Name the blood parasite species.
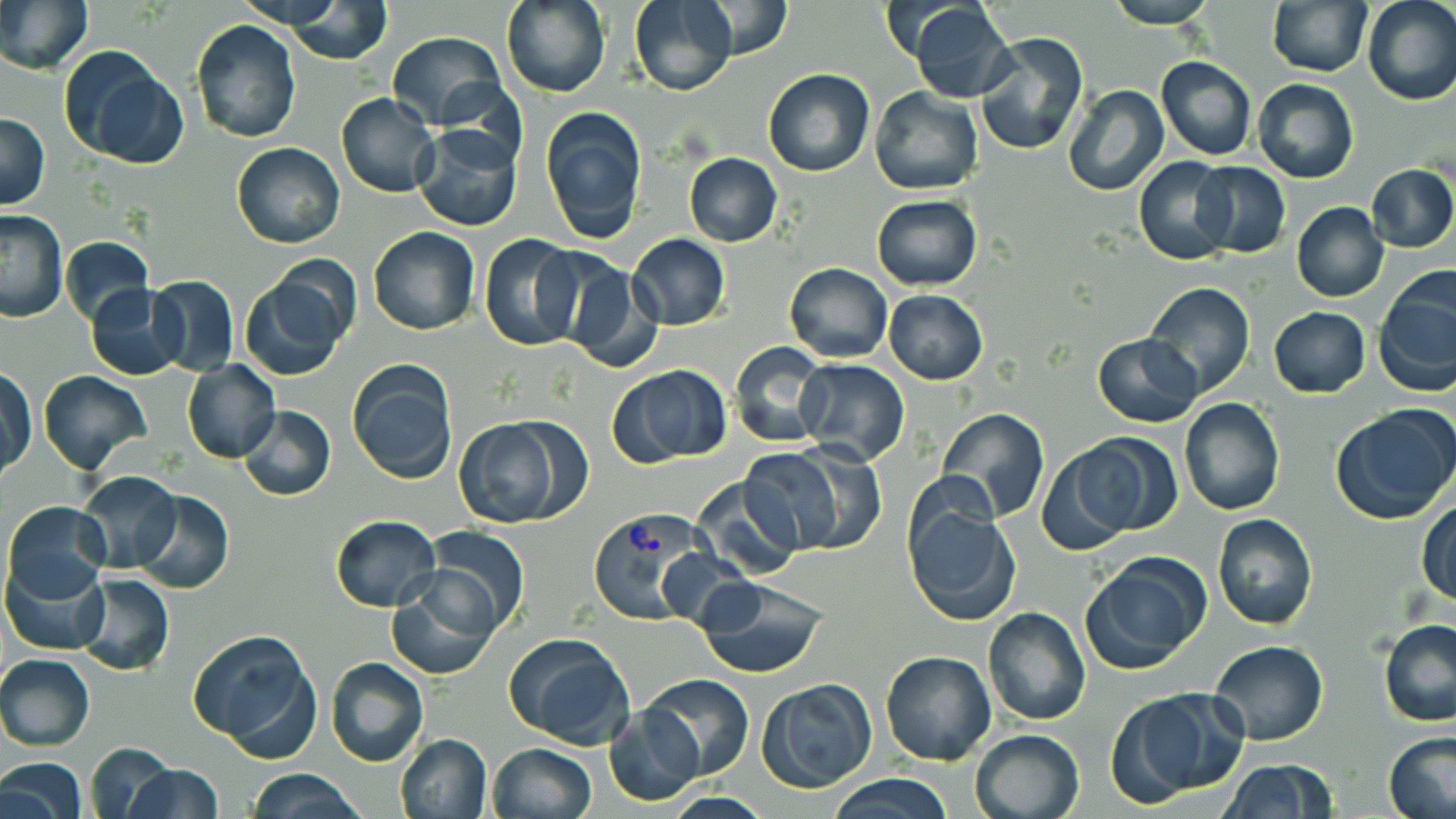
Plasmodium vivax.

Approximate bounding boxes as [x1, y1, x2, y2] in pixels. Uninfected red blood cell locations: [0, 0, 91, 75], [231, 0, 355, 32], [500, 0, 611, 98], [629, 0, 738, 95], [1103, 0, 1218, 27], [1361, 0, 1455, 107], [692, 1, 792, 62], [907, 1, 1019, 103], [1267, 1, 1372, 76], [285, 2, 390, 65], [191, 19, 301, 143], [386, 31, 507, 129], [975, 31, 1088, 156], [59, 47, 188, 169], [1155, 56, 1257, 160], [763, 67, 875, 177], [1252, 79, 1359, 185], [1064, 85, 1169, 198], [869, 86, 983, 195], [335, 92, 439, 198], [540, 106, 648, 243], [0, 112, 49, 209], [411, 124, 523, 232], [231, 141, 345, 249], [683, 152, 782, 247], [1133, 156, 1236, 266], [1192, 161, 1291, 258], [1367, 163, 1456, 253], [870, 195, 982, 289], [1291, 203, 1389, 302], [0, 211, 68, 323], [368, 226, 479, 335], [479, 232, 586, 351], [627, 233, 730, 331], [61, 237, 151, 326], [557, 260, 664, 373], [784, 263, 892, 362], [240, 273, 351, 380], [1375, 274, 1456, 399], [145, 275, 239, 374], [1143, 282, 1254, 398], [84, 284, 187, 381], [882, 289, 989, 384], [1268, 306, 1370, 398], [1092, 332, 1204, 427], [731, 343, 828, 448], [795, 358, 909, 465], [347, 360, 458, 483], [182, 361, 281, 464], [611, 364, 730, 467], [1, 367, 35, 479], [38, 370, 150, 474], [1179, 397, 1285, 515], [239, 404, 335, 500], [1332, 404, 1456, 524], [937, 409, 1048, 523], [456, 418, 573, 529], [1071, 433, 1184, 537], [777, 440, 888, 554], [1035, 446, 1136, 555], [739, 449, 849, 555], [74, 472, 181, 573], [690, 474, 803, 580], [134, 489, 234, 594], [903, 495, 1021, 626], [1415, 501, 1456, 606], [3, 502, 110, 605], [1211, 512, 1318, 630], [329, 514, 442, 612], [425, 526, 530, 634], [1080, 554, 1211, 674], [3, 557, 108, 655], [73, 573, 175, 675], [693, 576, 826, 679], [386, 577, 498, 680], [983, 607, 1090, 726], [1377, 619, 1456, 726], [188, 628, 321, 753], [507, 632, 637, 751], [1210, 640, 1328, 745], [880, 649, 997, 765], [0, 654, 95, 750], [325, 657, 429, 767], [642, 673, 754, 780], [756, 677, 878, 792], [1112, 689, 1247, 803], [605, 707, 703, 805], [970, 728, 1086, 819], [1385, 732, 1456, 819], [393, 733, 492, 819], [84, 741, 181, 819], [489, 744, 597, 819], [0, 756, 88, 819], [1216, 759, 1339, 818], [123, 763, 224, 819], [242, 768, 364, 818], [825, 773, 959, 818]. Plasmodium vivax-infected red blood cell locations: [587, 507, 713, 624]. May-Grünwald-Giemsa-stained preparation. Image is 1456×819 pixels. Captured at 1000x magnification. Single field of view. Thin blood film. Optical microscopy.